Assess this cell for malaria.
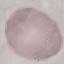

It is uninfected.

Summary:
  - Preparation: thin blood film
  - Capture: smartphone through the microscope eyepiece
  - Image type: cell patch, automatically extracted from a larger field of view and resized to 64 × 64 pixels
  - Stain: Giemsa